Outline each Plasmodium vivax-infected red blood cell.
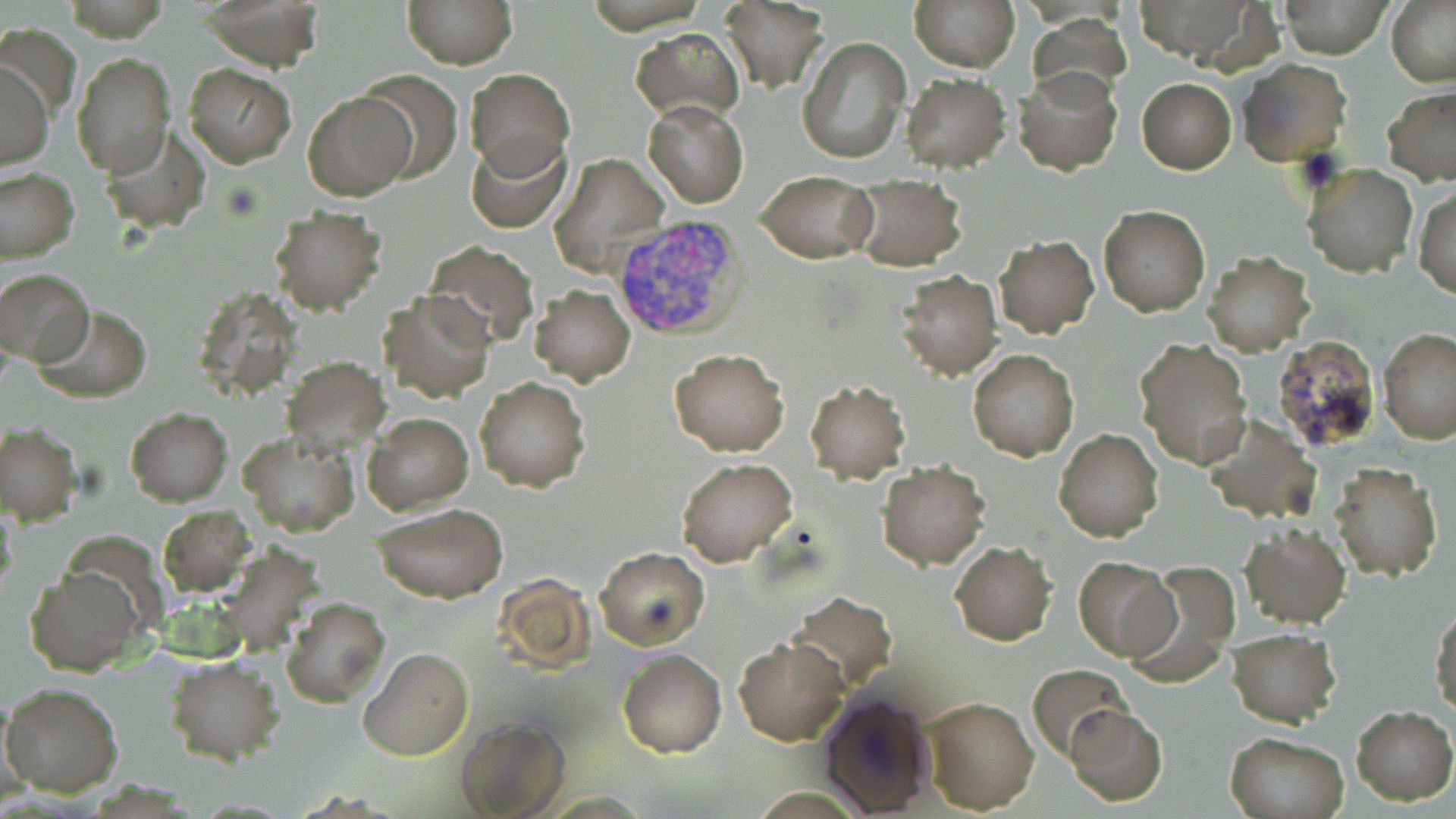
Approximate bounding boxes as (x1, y1, x2, y2) in pixels.
Plasmodium vivax-infected red blood cells: (612, 212, 750, 343).

Uninfected red blood cell locations: (204, 0, 325, 71), (402, 0, 516, 69), (720, 0, 831, 92), (910, 0, 1019, 72), (1278, 0, 1392, 58), (1387, 0, 1456, 87), (1028, 15, 1131, 102), (631, 29, 745, 122), (798, 37, 910, 164), (73, 53, 176, 176), (1236, 57, 1352, 167), (0, 61, 52, 170), (183, 63, 297, 169), (1013, 66, 1123, 175), (465, 68, 574, 176), (358, 71, 464, 183), (900, 72, 1012, 173), (1137, 78, 1236, 173), (1383, 86, 1456, 187), (302, 91, 416, 201), (644, 100, 748, 208), (99, 121, 209, 232), (466, 136, 570, 233), (551, 153, 668, 276), (1301, 163, 1417, 278), (0, 167, 78, 264), (757, 175, 877, 263), (847, 179, 967, 271), (1414, 186, 1456, 299), (1098, 205, 1211, 316), (267, 206, 385, 315), (994, 236, 1099, 337), (422, 242, 539, 347), (1203, 251, 1314, 357), (0, 267, 93, 366), (894, 271, 1002, 380), (528, 284, 635, 384), (379, 291, 493, 403), (35, 305, 151, 404), (1378, 327, 1456, 443), (1134, 338, 1253, 468), (670, 349, 789, 456), (969, 349, 1078, 461), (281, 358, 390, 455), (474, 377, 591, 492), (804, 380, 912, 484), (125, 408, 232, 506), (363, 413, 473, 514), (0, 425, 83, 526), (1055, 429, 1163, 541), (240, 431, 360, 537), (677, 458, 797, 568), (877, 461, 988, 570), (1330, 463, 1443, 582), (0, 500, 18, 599), (371, 503, 507, 602), (159, 506, 255, 596), (1240, 523, 1350, 628), (950, 541, 1058, 644), (593, 545, 709, 650), (1074, 556, 1178, 662), (1129, 562, 1240, 684), (24, 567, 145, 677), (788, 592, 896, 692), (281, 597, 390, 707), (1432, 605, 1455, 720), (1228, 628, 1341, 727), (734, 637, 850, 745), (359, 646, 474, 762), (618, 648, 726, 759), (163, 657, 286, 764), (1027, 665, 1132, 760), (1, 684, 123, 798), (817, 691, 938, 817), (922, 695, 1039, 815), (1064, 703, 1166, 805), (1351, 705, 1455, 805), (453, 713, 572, 819), (1224, 732, 1348, 819). Slide-level diagnosis: Plasmodium vivax. 1000x magnification. Single field of view. May-Grünwald-Giemsa stain. Light microscopy. Thin blood film. Image is 1456×819 pixels.